Report the malaria status of this cell.
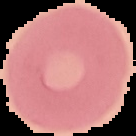

Uninfected.

The area outside the segmented cell region is set to black. Image is 136×136 pixels. From a thin blood smear.